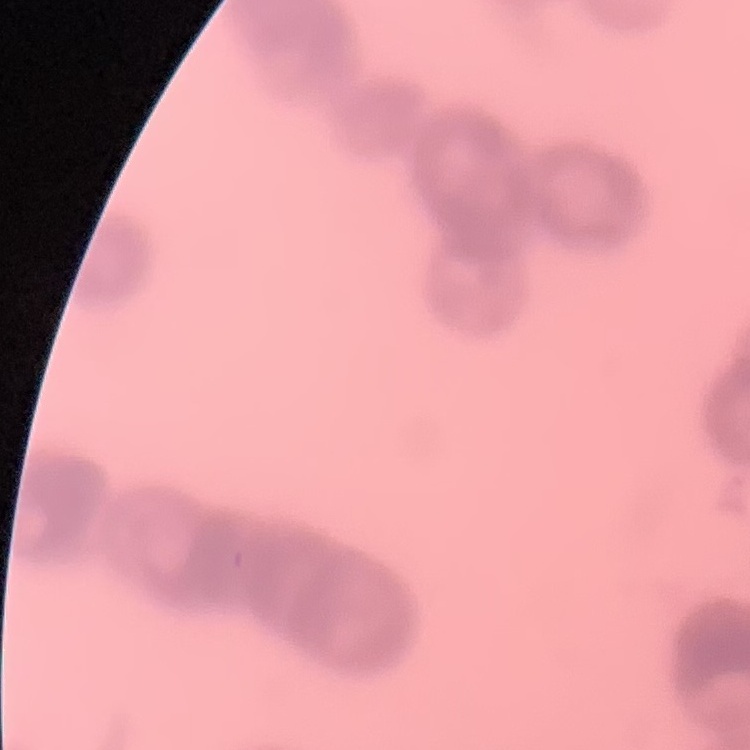

{
  "red_blood_cell_morphology": "rouleaux formation",
  "preparation": "thin blood film",
  "image_type": "square crop of a larger photomicrograph",
  "stain": "Field's or Giemsa"
}